Identify the blood parasite species.
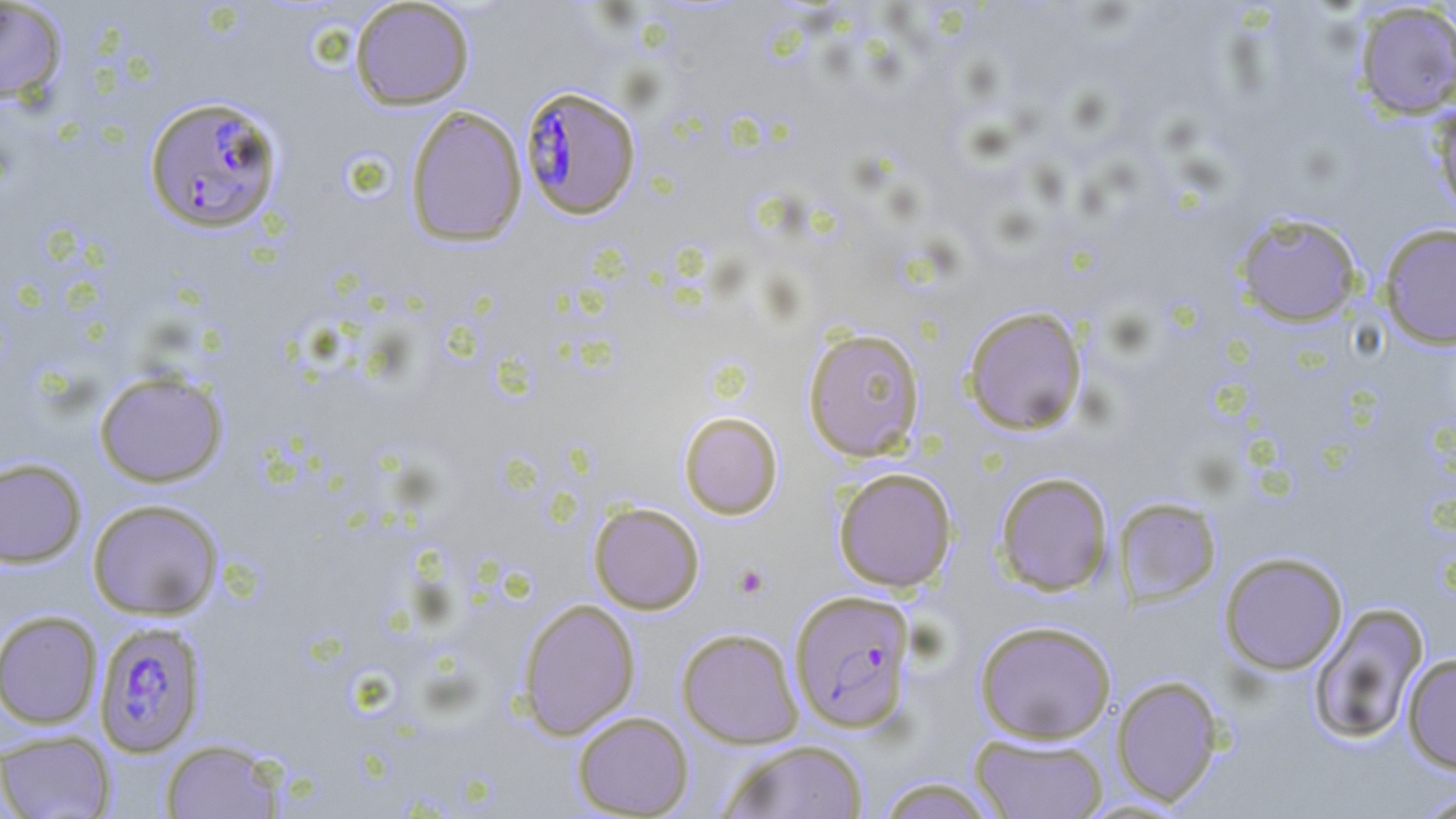

Plasmodium falciparum.

stain = May-Grünwald-Giemsa
image size = 1456×819 pixels
platelet locations = approximate bounding boxes as (x1, y1, x2, y2) in pixels: (732, 563, 769, 599)
modality = optical microscopy
Plasmodium falciparum-infected red blood cell locations = approximate bounding boxes as (x1, y1, x2, y2) in pixels: (520, 85, 641, 220), (144, 95, 283, 233), (789, 589, 917, 733), (93, 620, 208, 757)
uninfected red blood cell locations = approximate bounding boxes as (x1, y1, x2, y2) in pixels: (350, 0, 475, 110), (0, 1, 68, 104), (1353, 3, 1456, 120), (1430, 103, 1456, 219), (404, 105, 528, 247), (1232, 210, 1364, 327), (1379, 224, 1456, 349), (962, 305, 1088, 436), (802, 327, 926, 462), (93, 369, 229, 488), (678, 411, 783, 519), (0, 457, 87, 567), (832, 466, 958, 593), (994, 471, 1114, 596), (1113, 496, 1222, 606), (87, 498, 224, 620), (588, 502, 705, 614), (1219, 551, 1348, 674), (517, 598, 640, 739), (1308, 602, 1429, 746), (1, 610, 103, 729), (974, 620, 1117, 744), (676, 627, 804, 748), (1402, 652, 1456, 774), (1111, 675, 1225, 807), (572, 711, 694, 818), (0, 730, 116, 818), (970, 733, 1109, 818), (159, 738, 285, 818), (717, 740, 870, 819), (872, 776, 1003, 819), (1411, 788, 1456, 818)
magnification = 1000x
field of view = one of a larger specimen
preparation = thin blood film